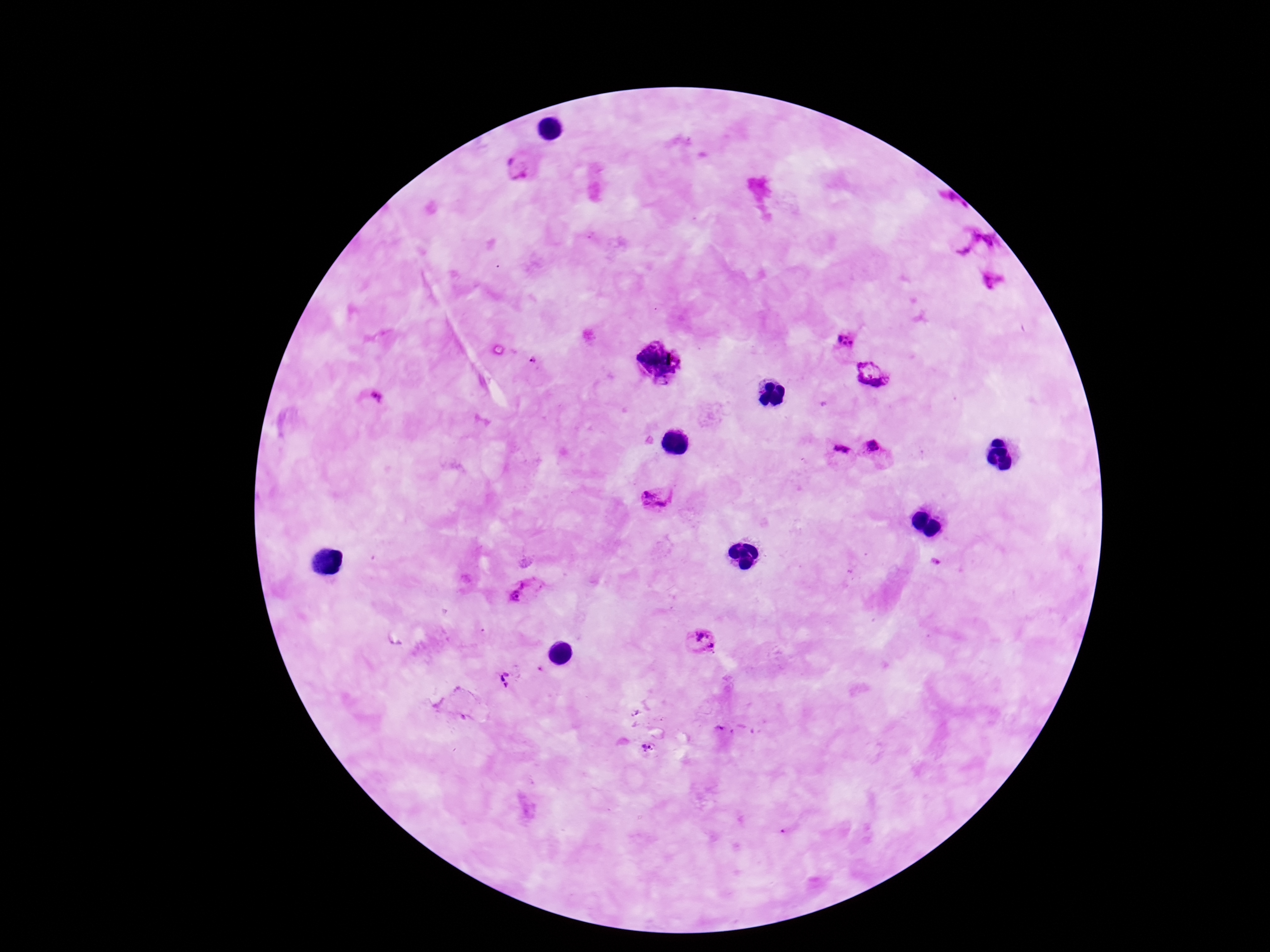
Approximate centers as [x, y] in pixels. Plasmodium parasite locations: [519, 166], [963, 235], [991, 243], [845, 339], [534, 360], [660, 361], [874, 375], [375, 396], [874, 450], [840, 454], [655, 498], [935, 561], [522, 593], [700, 642], [507, 679], [646, 747]. Photographed through the microscope eyepiece with a smartphone camera. Giemsa stain. 100x magnification. Single field of view. Patient malaria status: infected. Thick peripheral-blood smear. Image is 1270×952 pixels.